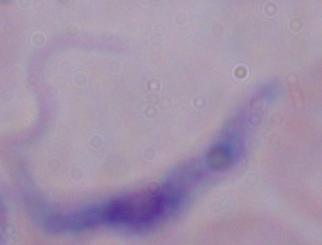

identification = trypanosome
modality = photomicrograph
magnification = 1000x